Classify this cell by malaria status.
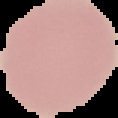

It is uninfected.

Summary:
  - Preparation: thin blood film
  - Image type: segmented cell region on a black background
  - Image size: 118×118 pixels